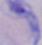 A trypanosome is seen. Micrograph. Captured at 1000x magnification.